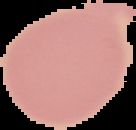

From a thin blood film. Malaria status: uninfected. Image is 136×130 pixels. Segmented cell region on a black background.